Locate every Plasmodium parasite.
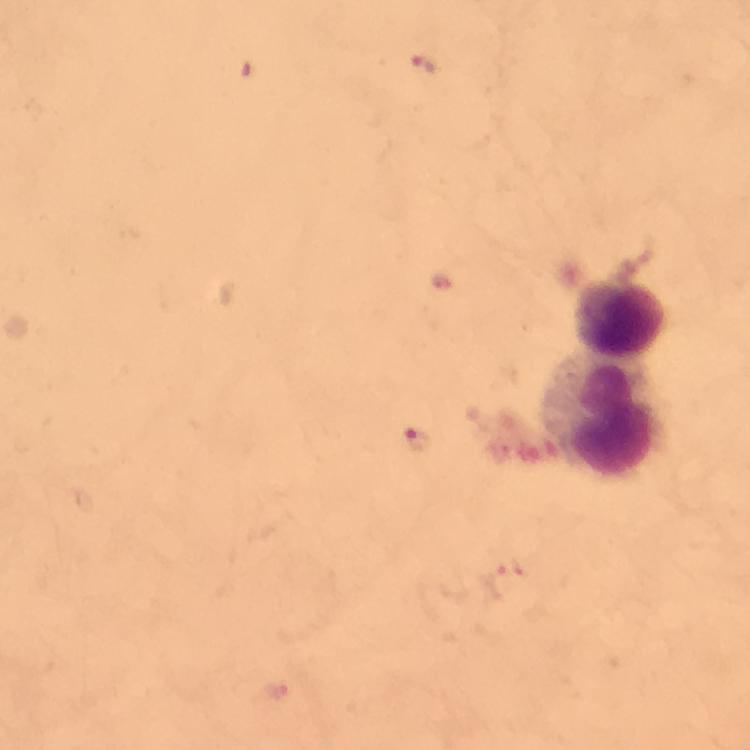

Approximate centers as (x, y) in pixels.
Plasmodium parasites: (425, 68), (418, 440), (505, 583), (278, 692).

cropped from = a single field of view
leukocyte locations = approximate centers as (x, y) in pixels: (619, 317), (609, 423)
preparation = thick smear
magnification = 100x
immersion oil = applied
capture = smartphone camera through the microscope
context = from a diagnostic examination for malaria
image size = 750×750 pixels
stain = Giemsa